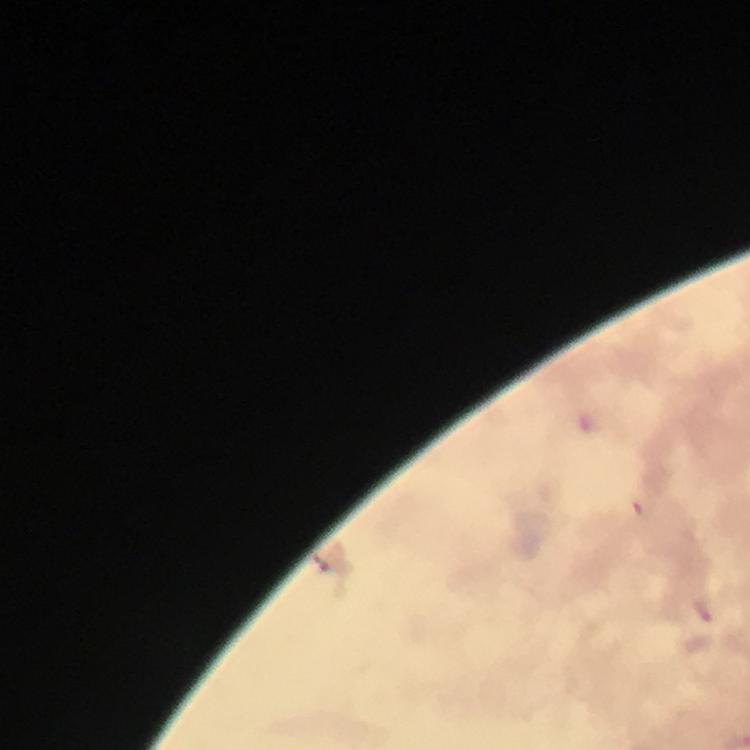

Approximate centers as {x, y} in pixels. Malaria parasite locations: {590, 426}, {640, 511}, {704, 610}. Immersion oil applied. Photographed with a smartphone mounted on the microscope. Giemsa-stained preparation. Image is 750×750 pixels. At 100x magnification. A crop from one field of view. From a malaria diagnostic workup. Thick smear.